Assess the morphology of the red blood cells.
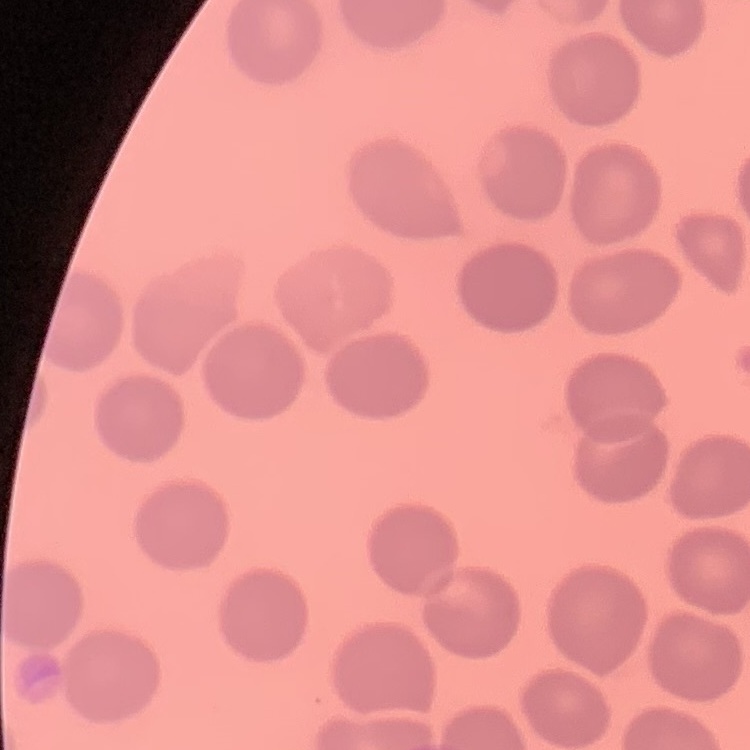

No rouleaux formation.

{
  "preparation": "thin blood film",
  "image_type": "square crop of a larger photomicrograph",
  "stain": "Field's or Giemsa"
}